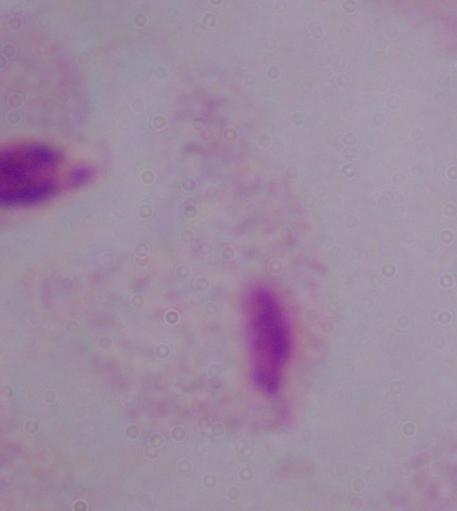

identification: trichomonad
magnification: 1000x
modality: photomicrograph